Name the blood parasite species.
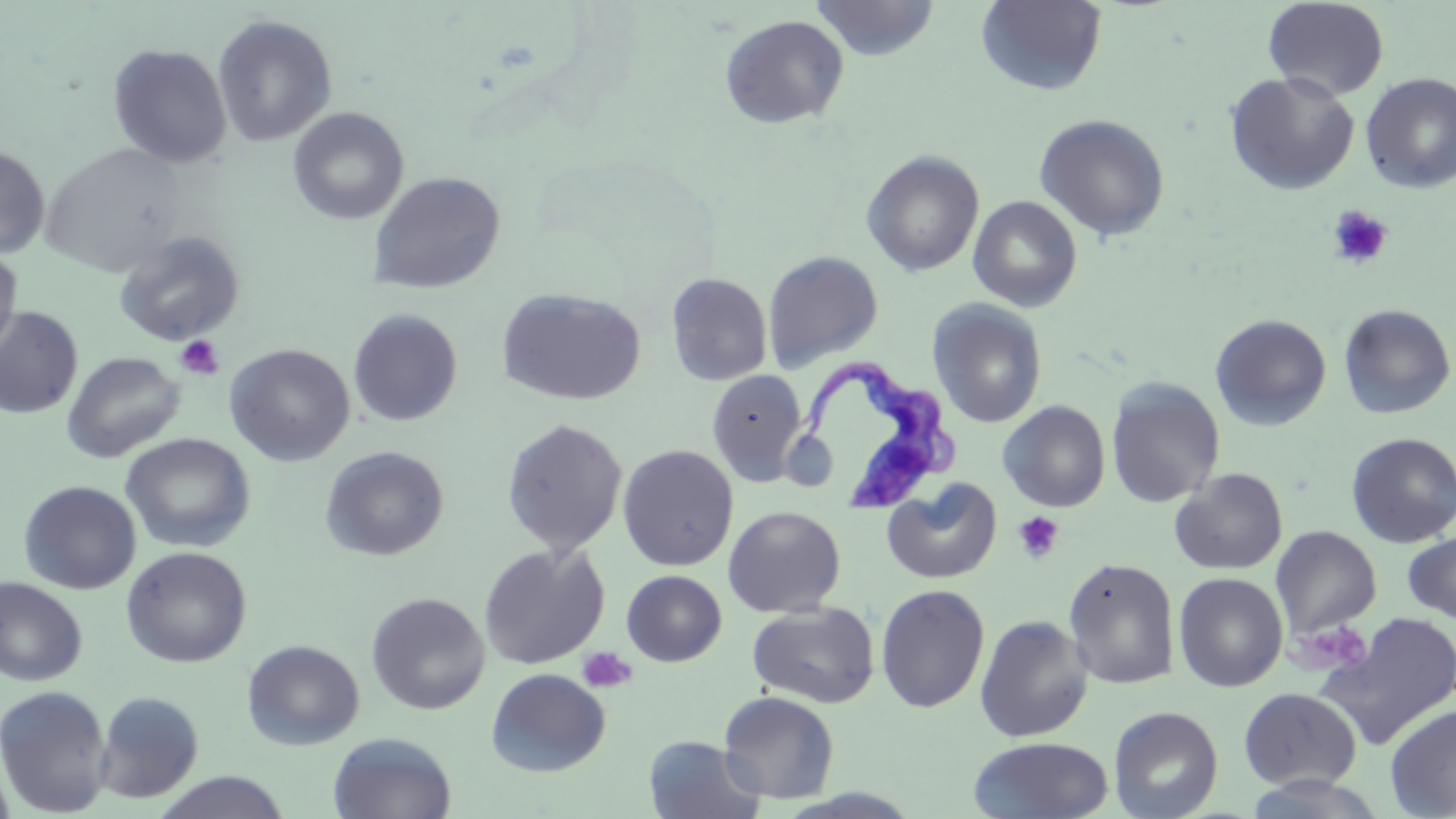
Trypanosoma brucei.

Summary:
  - Coordinate format: approximate bounding boxes as (x1, y1, x2, y2) in pixels
  - Uninfected red blood cell locations: (811, 0, 940, 61), (1263, 0, 1389, 101), (976, 1, 1107, 96), (212, 13, 338, 148), (719, 14, 848, 129), (107, 44, 232, 168), (1224, 71, 1360, 195), (1360, 72, 1456, 194), (287, 107, 409, 226), (1034, 114, 1171, 241), (40, 144, 187, 276), (0, 145, 49, 259), (861, 150, 985, 277), (367, 171, 506, 294), (968, 195, 1083, 312), (113, 230, 245, 346), (0, 247, 21, 360), (762, 250, 884, 372), (666, 272, 772, 386), (496, 287, 646, 406), (928, 299, 1047, 428), (1338, 304, 1456, 419), (0, 307, 83, 419), (348, 308, 463, 426), (1209, 313, 1332, 431), (224, 344, 355, 466), (61, 351, 185, 463), (706, 370, 807, 486), (1105, 377, 1226, 508), (998, 400, 1110, 512), (500, 419, 628, 557), (1345, 432, 1456, 548), (121, 433, 255, 553), (617, 445, 739, 571), (319, 446, 448, 561), (1170, 468, 1288, 575), (881, 479, 1002, 584), (19, 481, 141, 594), (722, 506, 846, 618), (1271, 525, 1381, 641), (1402, 527, 1456, 626), (477, 543, 610, 669), (121, 546, 251, 667), (1063, 558, 1181, 689), (622, 570, 727, 666), (1173, 572, 1288, 692), (0, 577, 87, 687), (875, 583, 990, 714), (365, 592, 489, 715), (747, 602, 880, 709), (1310, 612, 1456, 749), (974, 614, 1094, 742), (242, 639, 364, 750), (486, 668, 610, 777), (0, 685, 112, 816), (1238, 687, 1362, 791), (93, 691, 204, 803), (718, 691, 840, 804), (1385, 705, 1456, 818), (1109, 706, 1224, 819), (327, 732, 457, 819), (643, 735, 765, 819), (968, 736, 1114, 818), (0, 758, 16, 819), (153, 771, 290, 819)
  - Trypanosoma brucei locations: (798, 358, 961, 514)
  - Platelet locations: (1327, 205, 1393, 269), (175, 335, 224, 380), (1011, 511, 1064, 564), (1290, 619, 1373, 674), (577, 647, 636, 693)
  - Magnification: 1000x
  - Preparation: thin blood smear
  - Modality: optical microscopy
  - Stain: May-Grünwald-Giemsa
  - Field of view: single
  - Image size: 1456×819 pixels